Name the parasite shown.
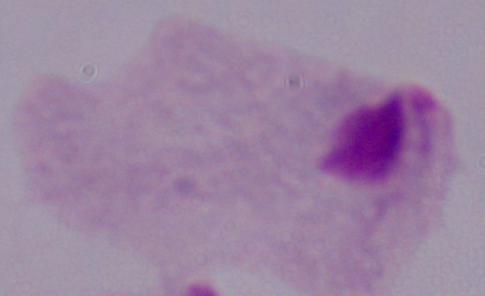

A trichomonad.

Photomicrograph. 1000x magnification.